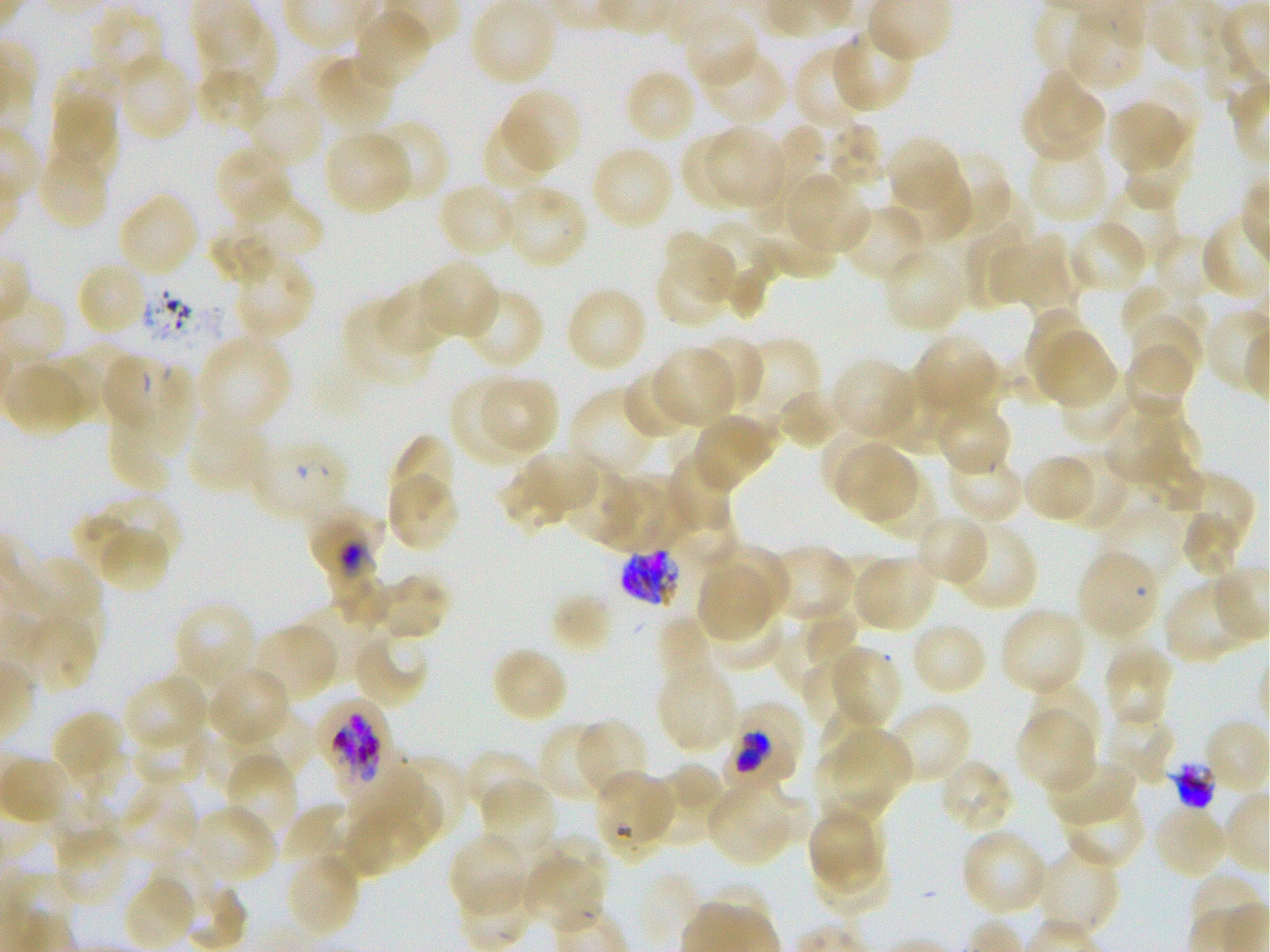
Approximate bounding boxes as [x1, y1, x2, y2] in pixels. Not every red blood cell is marked. A life-cycle stage — or a range of stages, where the recorded stages span more than one — follows each staged infected red blood cell.
Summary:
  - Locations of uninfected red blood cells: [471, 0, 556, 86], [1065, 7, 1146, 92], [89, 8, 166, 90], [353, 10, 431, 88], [683, 12, 758, 88], [201, 16, 276, 95], [829, 27, 914, 113], [794, 45, 868, 130], [704, 50, 787, 125], [117, 52, 196, 142], [314, 55, 396, 131], [51, 63, 121, 128], [194, 68, 268, 132], [623, 69, 697, 144], [1038, 70, 1105, 141], [503, 89, 582, 171], [245, 90, 323, 168], [54, 95, 119, 161], [1109, 100, 1186, 175], [1020, 102, 1104, 163], [482, 118, 556, 190], [368, 119, 448, 201], [828, 123, 886, 194], [748, 126, 829, 232], [710, 127, 783, 206], [323, 130, 412, 215], [44, 131, 123, 181], [680, 134, 753, 210], [886, 135, 961, 211], [1125, 143, 1192, 210], [215, 144, 292, 224], [590, 144, 674, 230], [1026, 145, 1108, 222], [40, 149, 108, 229], [930, 152, 1010, 233], [890, 165, 971, 244], [786, 175, 869, 255], [1101, 181, 1180, 266], [438, 183, 518, 258], [501, 185, 588, 269], [947, 187, 1034, 263], [118, 191, 199, 277], [239, 191, 322, 262], [842, 204, 927, 282], [701, 220, 780, 305], [1068, 220, 1149, 295], [965, 222, 1030, 310], [206, 224, 278, 286], [750, 229, 838, 276], [661, 231, 726, 289], [1152, 232, 1214, 298], [989, 233, 1071, 309], [882, 250, 963, 330], [656, 252, 732, 326], [235, 253, 316, 337], [420, 259, 500, 339], [723, 263, 771, 321], [81, 265, 143, 332], [1120, 284, 1207, 345], [376, 285, 449, 353], [462, 286, 545, 371], [565, 286, 649, 372], [342, 301, 436, 389], [1026, 308, 1097, 382], [1129, 315, 1203, 392], [913, 333, 1001, 417], [197, 334, 291, 434], [1038, 334, 1116, 408], [696, 335, 764, 411], [741, 338, 820, 427], [73, 340, 139, 416], [1124, 343, 1193, 420], [654, 347, 733, 427], [30, 356, 102, 423], [831, 357, 918, 440], [3, 360, 88, 436], [621, 368, 692, 441], [881, 369, 963, 453], [1057, 372, 1134, 444], [479, 375, 557, 455], [449, 379, 524, 464], [570, 386, 658, 478], [778, 389, 842, 450], [933, 400, 1013, 477], [1137, 400, 1203, 468], [1101, 406, 1182, 480], [107, 411, 172, 492], [189, 413, 265, 493], [693, 413, 774, 488], [822, 432, 885, 494], [390, 434, 456, 508], [834, 443, 891, 509], [526, 449, 598, 509], [1061, 449, 1130, 532], [664, 452, 735, 535], [947, 453, 1026, 524], [1022, 453, 1095, 524], [860, 455, 916, 522], [1141, 456, 1204, 515], [562, 465, 641, 549], [496, 467, 564, 535], [869, 471, 940, 541], [1176, 471, 1255, 556], [386, 474, 460, 552], [604, 476, 683, 552], [98, 494, 181, 566], [672, 502, 737, 568], [72, 508, 150, 580], [1100, 508, 1183, 586], [1180, 509, 1245, 578], [915, 513, 990, 587], [952, 521, 1039, 612], [98, 527, 169, 594], [771, 545, 855, 622], [705, 547, 789, 619], [825, 554, 882, 628], [853, 555, 938, 633], [25, 556, 101, 636], [698, 568, 771, 637], [331, 572, 391, 629], [377, 574, 451, 641], [1162, 579, 1249, 664], [550, 591, 614, 652], [300, 600, 381, 679], [172, 601, 258, 691], [706, 603, 784, 670], [803, 606, 860, 667], [1000, 606, 1087, 696], [16, 612, 98, 694], [655, 617, 714, 690], [910, 621, 988, 696], [253, 623, 337, 702], [776, 629, 856, 694], [351, 632, 429, 709], [1104, 644, 1172, 728], [826, 645, 901, 730], [491, 647, 569, 724], [168, 648, 258, 726], [800, 658, 867, 723], [657, 663, 739, 753], [210, 665, 291, 746], [124, 675, 209, 751], [1027, 677, 1101, 753], [821, 701, 887, 771], [885, 702, 972, 785], [732, 704, 804, 767], [1102, 705, 1178, 785], [229, 708, 314, 783], [54, 710, 123, 778], [1016, 711, 1096, 794], [576, 719, 647, 802], [131, 720, 209, 786], [538, 722, 613, 803], [834, 732, 910, 813], [203, 734, 279, 794], [69, 741, 134, 803], [814, 747, 886, 828], [461, 748, 541, 821], [228, 754, 296, 833], [393, 754, 469, 840], [1048, 757, 1136, 827], [939, 758, 1015, 835], [643, 762, 724, 845], [343, 771, 424, 825], [593, 771, 674, 847], [733, 774, 811, 843], [373, 778, 442, 845], [480, 779, 556, 861], [120, 784, 196, 862], [706, 787, 789, 864], [1061, 790, 1146, 869], [52, 797, 118, 851], [280, 803, 346, 863], [190, 805, 277, 885], [1151, 806, 1229, 879], [346, 811, 422, 878], [808, 812, 879, 896], [53, 828, 130, 906], [961, 829, 1048, 917], [447, 832, 530, 916], [540, 832, 611, 907], [1036, 846, 1119, 936], [813, 848, 893, 915], [285, 852, 361, 938], [524, 853, 602, 930], [149, 854, 220, 932], [123, 875, 196, 949], [185, 884, 249, 948]
  - Locations of red blood cells of indeterminate infection status: [101, 353, 153, 428], [153, 357, 195, 443], [1077, 550, 1160, 639], [316, 697, 392, 790], [725, 720, 796, 792]
  - Locations of infected red blood cells: [248, 436, 351, 522] ring; [308, 508, 384, 590] trophozoite; [620, 547, 681, 607]
  - Life-cycle stages observed: ring, trophozoite
  - Stain: Giemsa
  - Image size: 1270×952 pixels
  - Preparation: thin blood film
  - Donor blood group: O+
  - Objective: 100x, oil immersion, numerical aperture 1.25
  - Culture: in-vitro Plasmodium falciparum strain 3D7, static
  - Field of view: single